Report the malaria status of this cell.
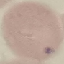

It is uninfected.

Photographed with a smartphone camera at the microscope eyepiece. Thin smear of blood. Automatically extracted cell patch, resized to 64 × 64 pixels. Giemsa stain.